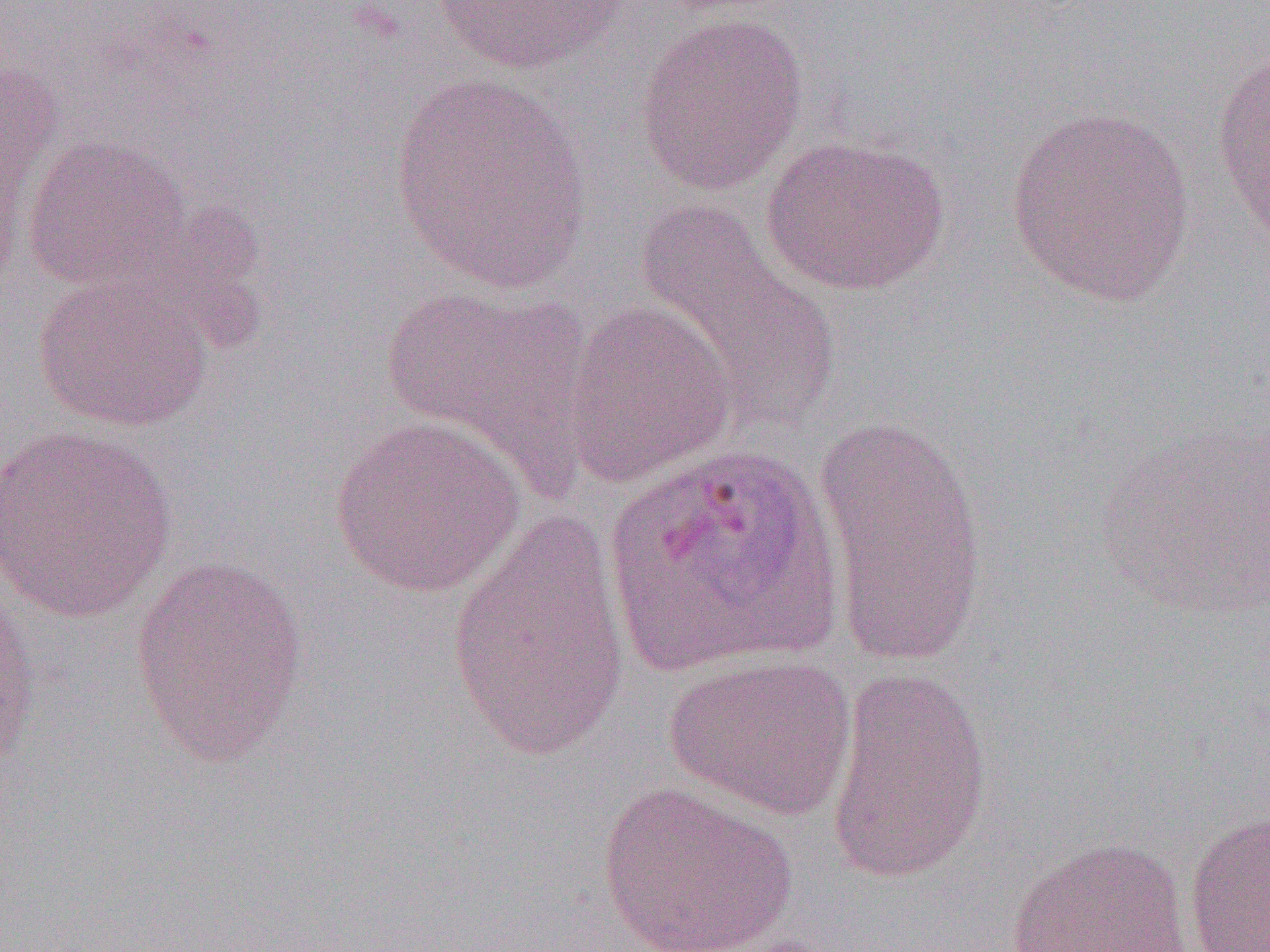

Summary:
  - Coordinate format: approximate bounding boxes as [x1, y1, x2, y2] in pixels
  - Plasmodium ovale-infected red blood cell locations: [602, 441, 843, 679]
  - Uninfected red blood cell locations: [430, 0, 629, 76], [635, 12, 809, 195], [1209, 43, 1269, 248], [0, 51, 64, 261], [390, 75, 594, 293], [1004, 104, 1198, 305], [21, 134, 194, 293], [760, 134, 949, 296], [632, 200, 844, 429], [33, 272, 212, 432], [378, 283, 594, 487], [561, 299, 737, 487], [813, 411, 991, 668], [329, 414, 527, 598], [1093, 421, 1270, 620], [0, 424, 179, 621], [446, 509, 632, 764], [127, 554, 310, 766], [0, 571, 41, 790], [663, 652, 857, 819], [825, 666, 993, 888], [596, 780, 798, 952], [1183, 808, 1269, 952], [1006, 835, 1193, 952]
  - Slide-level diagnosis: Plasmodium ovale
  - Image size: 1270×952 pixels
  - Field of view: single
  - Modality: optical microscopy
  - Preparation: thin blood smear
  - Magnification: 1000x